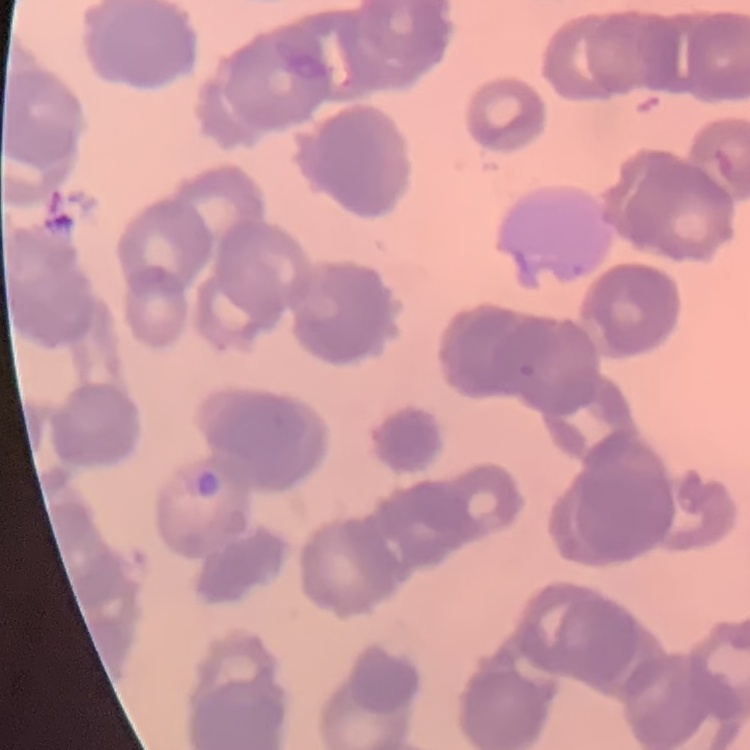

The erythrocytes exhibit rouleaux formation. One tile cut from a larger photomicrograph. Stained with either Field's or Giemsa. Thin blood smear.